Describe the morphology of the red blood cells.
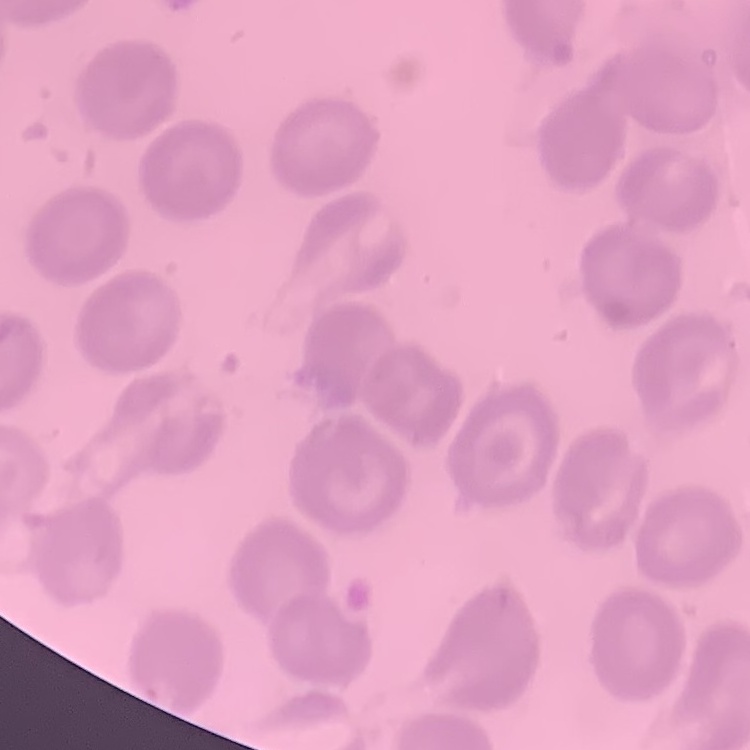
No rouleaux formation.

Summary:
  - Image type: square crop of a larger photomicrograph
  - Preparation: thin peripheral smear
  - Stain: Field's or Giemsa